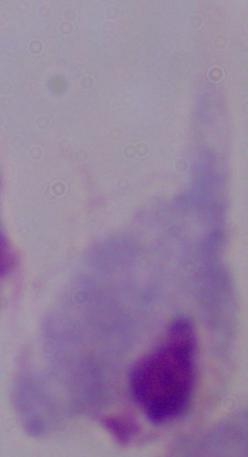 1000x magnification. Photomicrograph. A trichomonad is seen.